Give the position of every leukocyte visible.
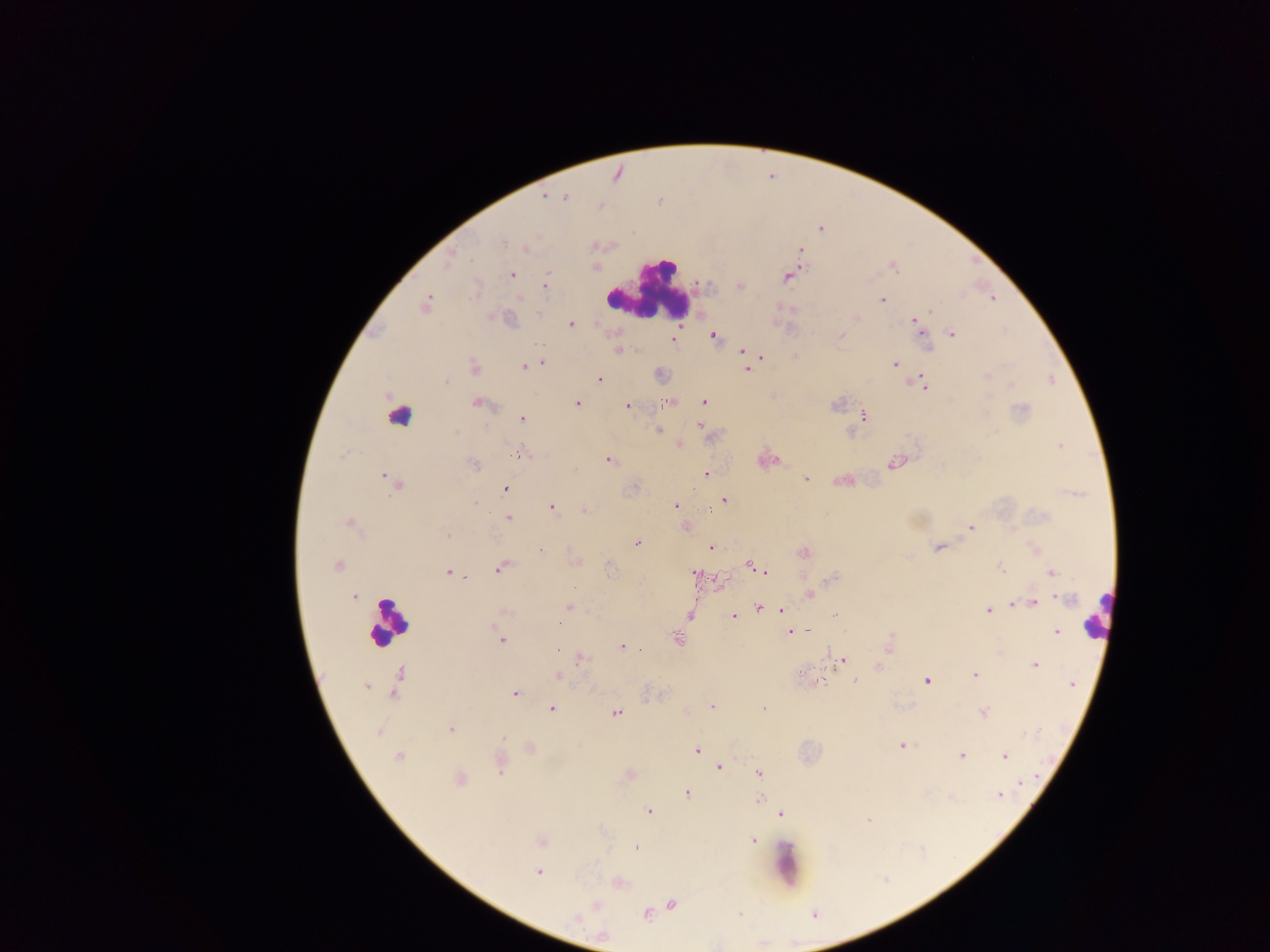

Approximate centers as (x, y) in pixels.
Leukocytes: (647, 290), (401, 418), (1098, 614), (387, 621), (788, 867).

Summary:
  - Malaria parasite locations: (543, 197), (565, 197), (820, 229), (502, 242), (528, 249), (448, 261), (893, 267), (512, 274), (788, 277), (546, 285), (740, 285), (993, 298), (522, 299), (882, 299), (425, 305), (509, 319), (858, 319), (915, 320), (570, 325), (713, 335), (841, 335), (953, 335), (925, 336), (673, 339), (618, 350), (742, 351), (744, 356), (796, 356), (762, 357), (543, 363), (895, 364), (524, 366), (474, 368), (747, 369), (987, 376), (600, 380), (445, 381), (922, 383), (704, 402), (477, 403), (576, 403), (668, 403), (836, 405), (627, 406), (1022, 409), (863, 415), (522, 418), (700, 426), (658, 430), (679, 445), (1060, 445), (522, 453), (610, 460), (894, 463), (474, 464), (706, 473), (388, 479), (806, 479), (394, 483), (505, 489), (723, 500), (475, 503), (676, 506), (552, 508), (585, 510), (710, 510), (507, 517), (349, 525), (685, 527), (971, 527), (447, 536), (637, 543), (711, 548), (937, 548), (541, 551), (804, 552), (750, 565), (337, 566), (609, 566), (500, 568), (1001, 568), (759, 569), (448, 572), (1052, 572), (694, 573), (765, 573), (833, 578), (810, 595), (353, 597), (1066, 599), (1035, 601), (1023, 603), (1014, 605), (569, 608), (759, 608), (782, 610), (988, 610), (505, 611), (834, 615), (689, 616), (734, 617), (559, 625), (808, 631), (791, 632), (1056, 632), (891, 636), (677, 639), (501, 640), (889, 645), (621, 647), (557, 650), (582, 659), (843, 659), (878, 666), (1035, 666), (399, 673), (801, 673), (975, 675), (558, 676), (822, 681), (855, 681), (926, 681), (1072, 683), (366, 687), (394, 692), (515, 693), (766, 705), (713, 706), (551, 708), (983, 712), (617, 713), (451, 730), (378, 731), (504, 738), (902, 745), (697, 750), (962, 755), (1005, 756), (398, 757), (719, 767), (500, 768), (759, 772), (460, 780), (1022, 782), (687, 793), (1000, 796), (758, 800), (649, 811), (781, 814), (868, 819), (753, 840), (541, 842), (636, 848), (537, 872), (672, 904), (597, 905), (646, 915), (575, 918)
  - Field of view: single
  - Capture: mobile-phone photograph through a microscope
  - Country: Ghana
  - Image size: 1270×952 pixels
  - Preparation: thick blood film